Assess this cell for malaria.
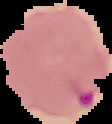

It is parasitized.

preparation = thin blood film
image size = 112×124 pixels
image type = segmented cell region with the area outside set to black